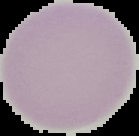

Summary:
  - Image type: segmented cell region on a black background
  - Malaria status: uninfected
  - Preparation: thin blood film
  - Image size: 139×136 pixels